Give the position of every malaria parasite.
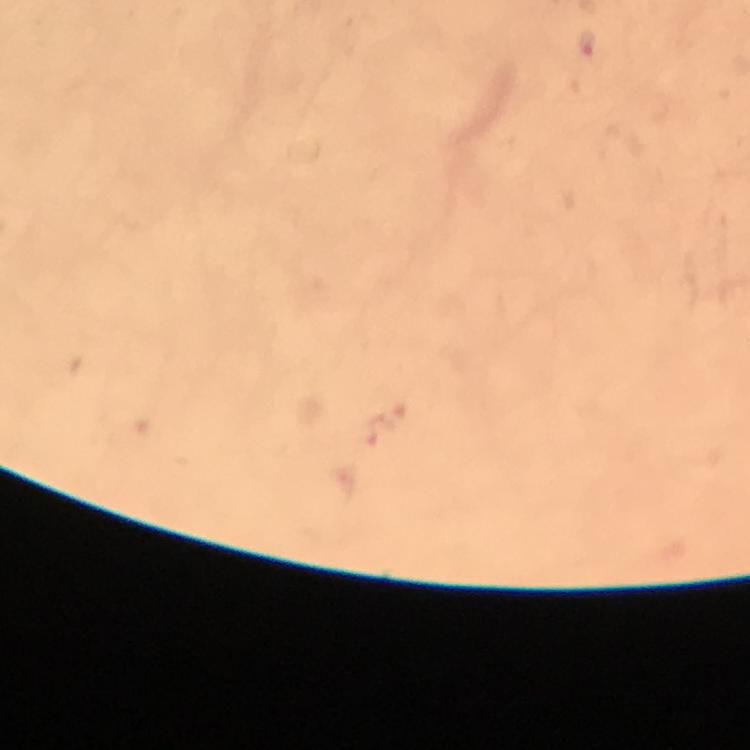

Approximate centers as [x, y] in pixels.
Malaria parasites: [587, 43].

context: from a diagnostic examination for malaria
magnification: 100x
preparation: thick blood film
stain: Giemsa
immersion_oil: applied
image_size: 750×750 pixels
capture: smartphone mounted on the microscope
cropped_from: a single field of view